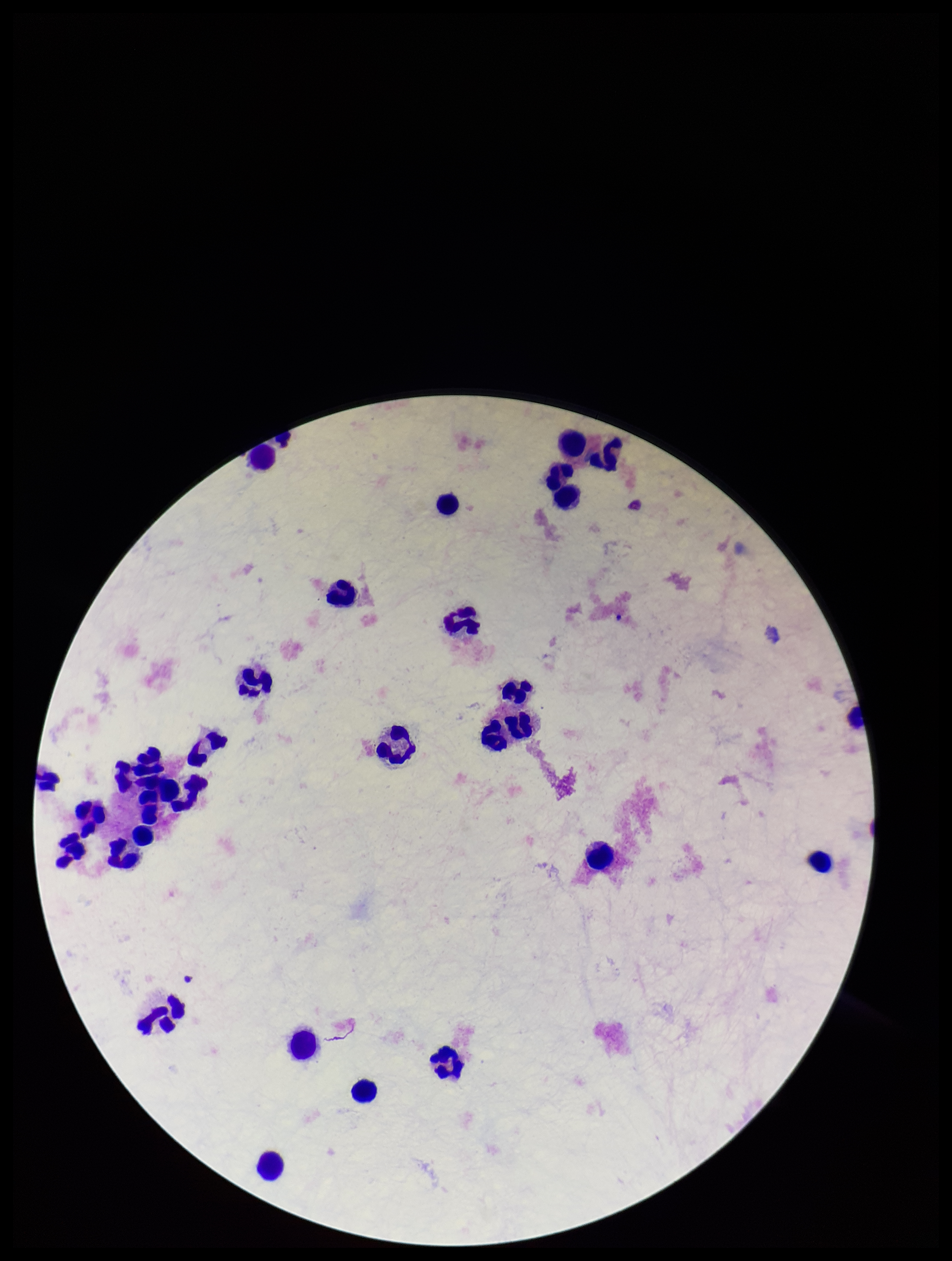
{
  "leukocyte_count": 28,
  "plasmodium_parasites": "none seen",
  "field_of_view": "one from this slide",
  "parasite_count": 0,
  "image_size": "952×1261 pixels",
  "capture": "smartphone photograph through the microscope eyepiece",
  "patient_malaria_status": "negative",
  "preparation": "thick blood smear",
  "stain": "Giemsa"
}